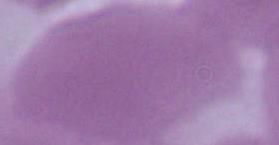 1000x magnification. Photomicrograph. A red blood cell is shown.